Outline each Babesia divergens-infected red blood cell.
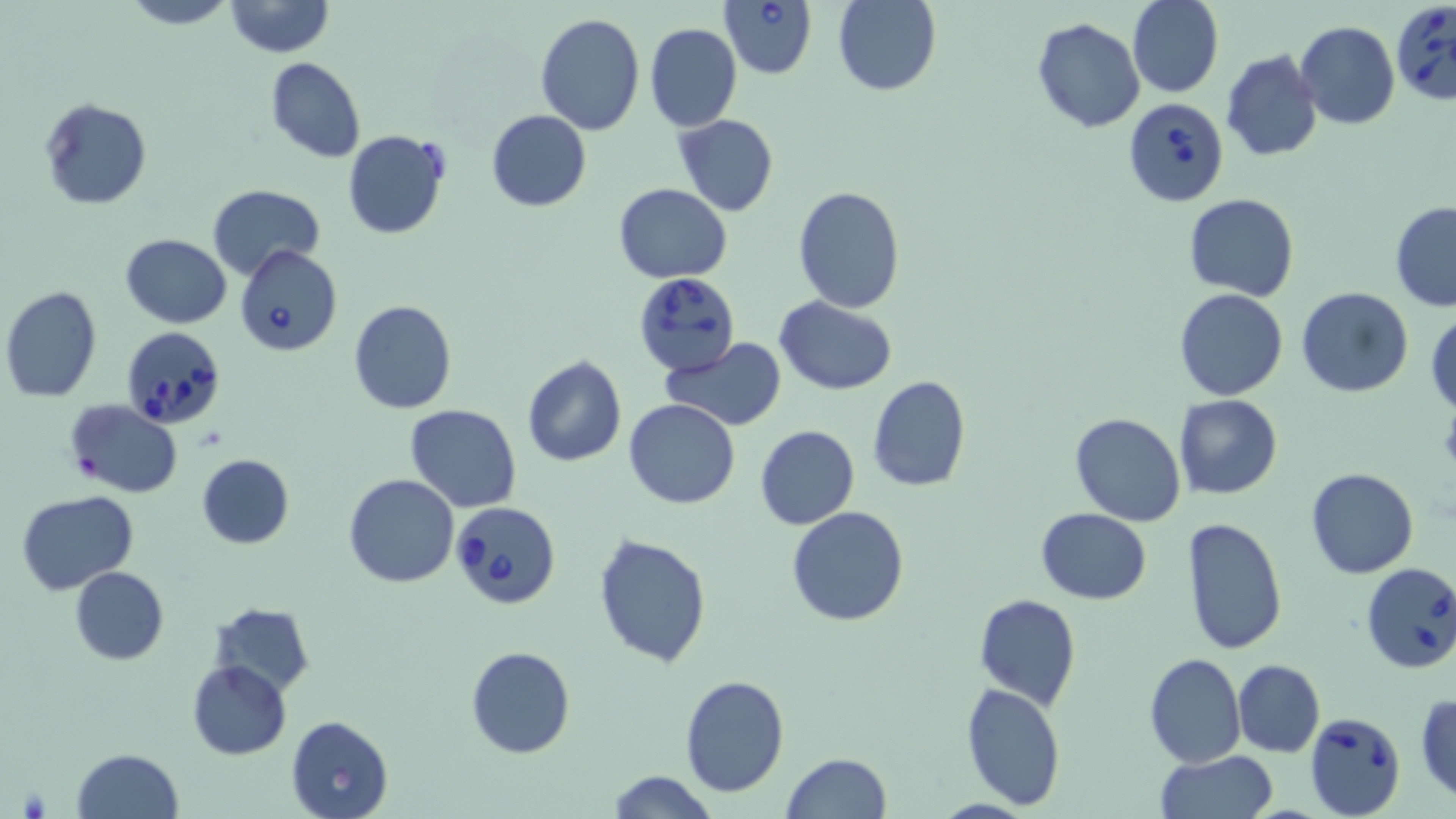

Approximate bounding boxes as (x1,y1)-(x2,y2) corner pairs in pixels.
Babesia divergens-infected red blood cells: (718,0)-(817,79), (1392,1)-(1456,103), (1124,97)-(1229,206), (236,246)-(342,355), (632,270)-(737,374), (120,324)-(226,431), (450,500)-(561,606), (1358,561)-(1456,674), (1304,711)-(1406,818).

Summary:
  - Uninfected red blood cell locations: (120,0)-(238,29), (223,0)-(332,57), (832,0)-(941,96), (1127,0)-(1223,98), (535,13)-(645,135), (1031,18)-(1145,133), (1296,22)-(1400,130), (645,23)-(742,132), (1221,49)-(1322,161), (265,56)-(365,164), (39,97)-(152,210), (485,110)-(592,211), (673,113)-(778,218), (341,132)-(449,239), (207,183)-(325,279), (614,183)-(733,283), (791,186)-(907,314), (1185,193)-(1298,300), (1390,203)-(1456,311), (120,234)-(231,328), (1,285)-(102,401), (1173,288)-(1288,401), (1298,288)-(1414,398), (774,296)-(898,395), (348,300)-(457,414), (1427,311)-(1456,415), (662,337)-(788,431), (522,357)-(627,469), (867,376)-(971,492), (1174,395)-(1283,500), (65,398)-(183,497), (624,398)-(741,508), (405,403)-(522,512), (1069,413)-(1186,526), (755,425)-(859,530), (196,452)-(294,549), (1305,467)-(1419,579), (343,474)-(459,588), (17,491)-(138,596), (786,505)-(910,626), (1035,506)-(1151,604), (1179,516)-(1287,657), (592,532)-(711,670), (71,566)-(168,665), (974,594)-(1080,709), (209,602)-(315,695), (466,646)-(575,759), (1144,652)-(1246,768), (1233,659)-(1325,756), (186,660)-(292,760), (679,675)-(790,798), (960,681)-(1067,810), (1414,691)-(1456,803), (285,714)-(393,818), (70,748)-(184,819), (1154,751)-(1277,819), (780,753)-(891,819), (608,771)-(720,818)
  - Platelet locations: (1439,402)-(1456,477), (18,786)-(49,815)
  - Slide-level diagnosis: Babesia divergens
  - Modality: light microscopy
  - Field of view: one of a larger specimen
  - Preparation: thin blood film
  - Magnification: 1000x
  - Stain: May-Grünwald-Giemsa
  - Image size: 1456×819 pixels